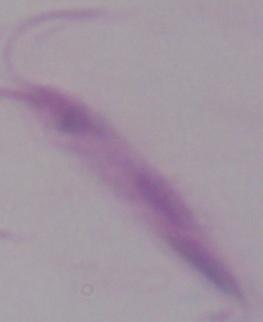 A Leishmania parasite is shown. Micrograph. 1000x magnification.